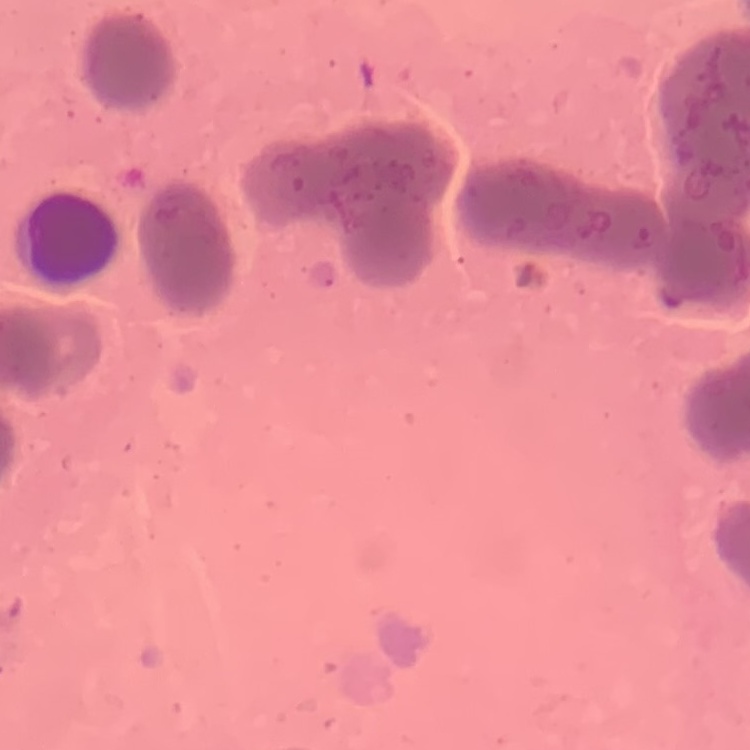
red blood cell morphology = rouleaux formation
stain = Field's or Giemsa
preparation = thin peripheral smear
image type = square crop of a larger photomicrograph